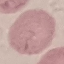

malaria status = uninfected
image type = cell patch, automatically extracted from a larger field of view and resized to 64 × 64 pixels
preparation = thin smear
stain = Giemsa
capture = smartphone through the microscope eyepiece